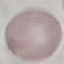

Summary:
  - Malaria status: uninfected
  - Capture: smartphone through the microscope eyepiece
  - Preparation: thin smear
  - Stain: Giemsa
  - Image type: cell patch, automatically extracted from a larger field of view and resized to 64 × 64 pixels